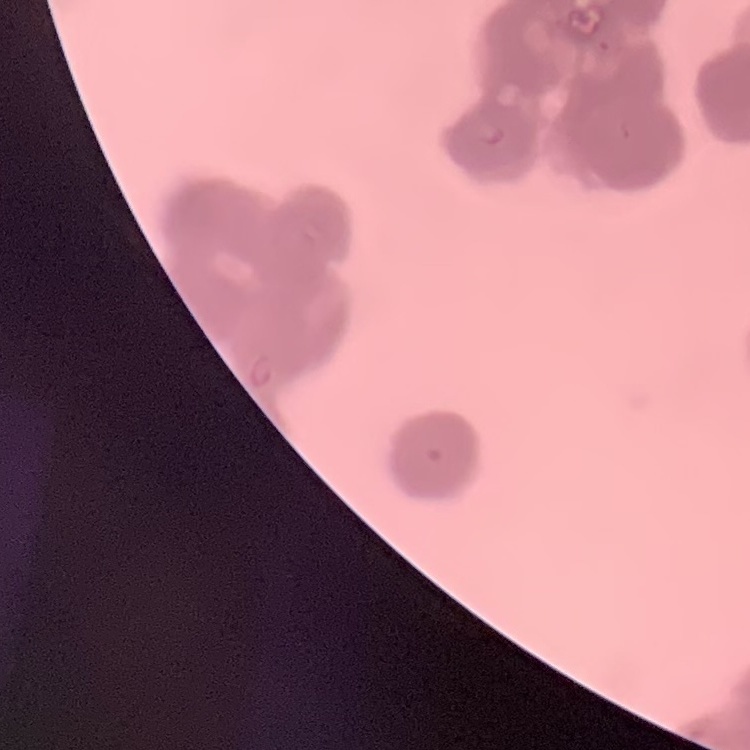

Summary:
  - Red blood cell morphology: rouleaux formation
  - Preparation: thin blood smear
  - Image type: one tile cut from a larger photomicrograph
  - Stain: Field's or Giemsa